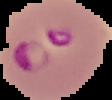
{
  "result": "Plasmodium parasites detected",
  "image_type": "segmented cell region with the area outside set to black",
  "image_size": "112×100 pixels",
  "preparation": "thin blood smear"
}